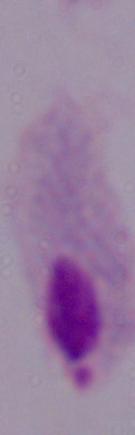

Summary:
  - Modality: photomicrograph
  - Magnification: 1000x
  - Identification: trichomonad